Name the parasite shown.
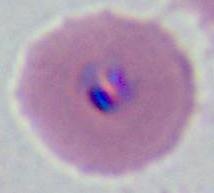
This is Plasmodium.

modality = photomicrograph
magnification = 400x or 1000x